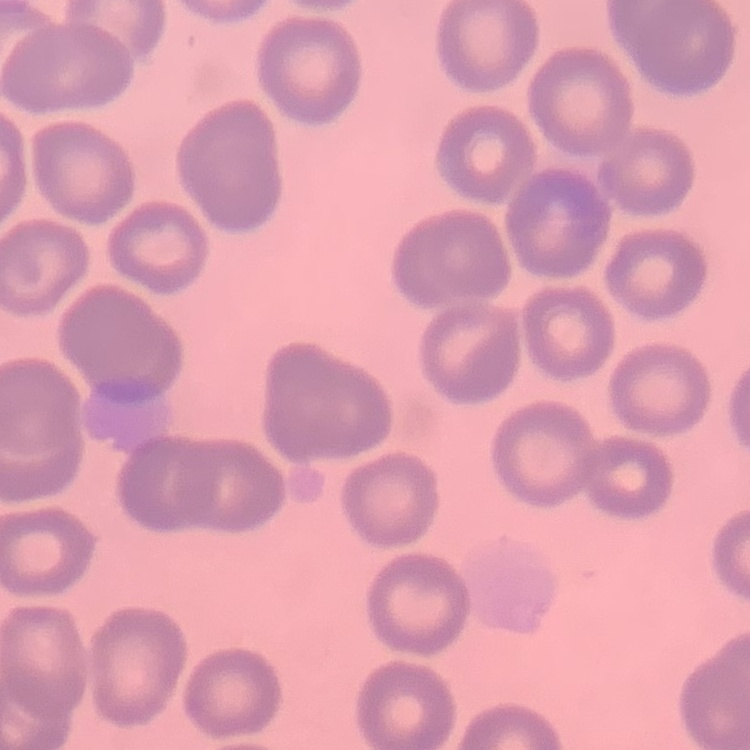

erythrocyte morphology = no rouleaux formation
preparation = thin blood smear
image type = one tile cut from a larger photomicrograph
stain = Field's or Giemsa